Locate and identify every blood parasite.
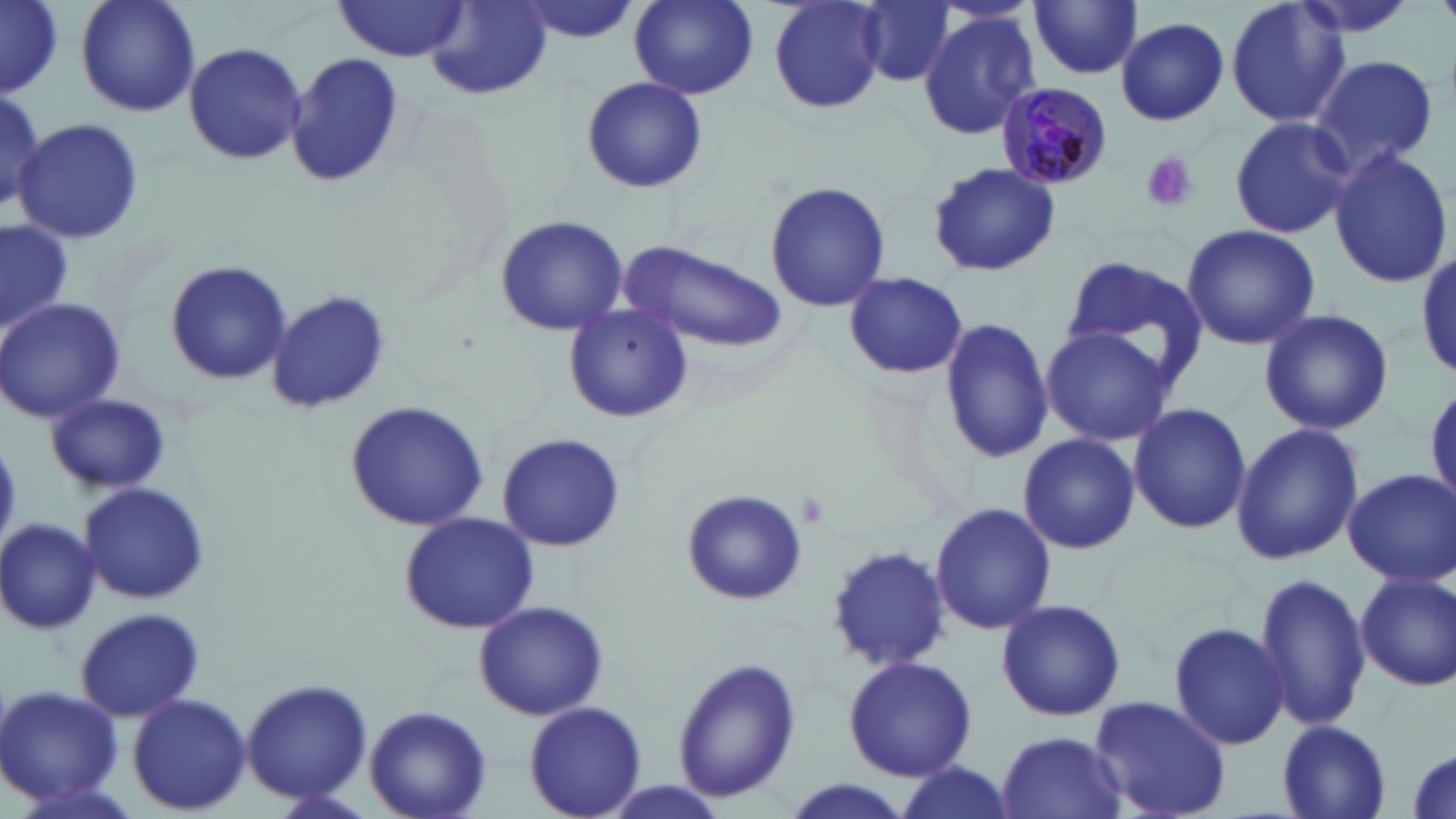
Approximate bounding boxes as (x1,y1)-(x2,y2) corner pairs in pixels.
Plasmodium malariae-infected red blood cells: (997,82)-(1115,191).
No Plasmodium falciparum, Plasmodium ovale, Plasmodium vivax, Babesia divergens, or Trypanosoma brucei observed.

Summary:
  - Platelet locations: (1141,151)-(1197,213)
  - Uninfected red blood cell locations: (1,0)-(60,95), (76,0)-(199,117), (510,0)-(641,43), (627,0)-(759,101), (1225,0)-(1351,131), (335,1)-(469,61), (857,1)-(956,86), (770,2)-(882,113), (1028,2)-(1143,79), (425,4)-(552,103), (917,9)-(1040,138), (1116,16)-(1229,126), (184,42)-(307,166), (289,52)-(405,187), (1308,54)-(1440,176), (581,76)-(706,194), (0,79)-(47,218), (1228,116)-(1358,240), (15,118)-(145,246), (1329,148)-(1454,288), (925,161)-(1060,279), (765,180)-(890,313), (494,214)-(628,335), (0,218)-(72,336), (1179,225)-(1320,352), (623,241)-(787,353), (1413,248)-(1456,378), (1060,254)-(1210,394), (166,261)-(292,384), (844,270)-(968,379), (266,289)-(390,415), (0,298)-(126,424), (561,303)-(692,424), (1258,308)-(1394,435), (937,315)-(1053,465), (1040,326)-(1172,445), (1427,378)-(1456,511), (46,394)-(171,495), (345,401)-(489,532), (1128,402)-(1251,535), (1231,422)-(1364,565), (498,435)-(624,549), (1016,436)-(1140,552), (1343,468)-(1456,586), (78,482)-(211,604), (681,488)-(807,607), (930,503)-(1057,635), (398,510)-(540,633), (0,516)-(100,632), (826,544)-(949,671), (1355,571)-(1456,692), (1252,572)-(1372,733), (996,598)-(1127,721), (473,600)-(608,720), (74,607)-(207,721), (1169,620)-(1289,752), (842,653)-(977,781), (670,657)-(802,806), (241,678)-(372,805), (1,684)-(125,811), (127,692)-(252,814), (1088,694)-(1232,819), (524,701)-(647,818), (366,705)-(492,819), (1276,720)-(1392,818), (996,731)-(1127,818), (1407,746)-(1454,817), (895,761)-(1016,816), (779,780)-(916,819)
  - Slide-level diagnosis: Plasmodium malariae
  - Magnification: 1000x
  - Image size: 1456×819 pixels
  - Stain: May-Grünwald-Giemsa
  - Modality: light microscopy
  - Field of view: single
  - Preparation: thin blood smear